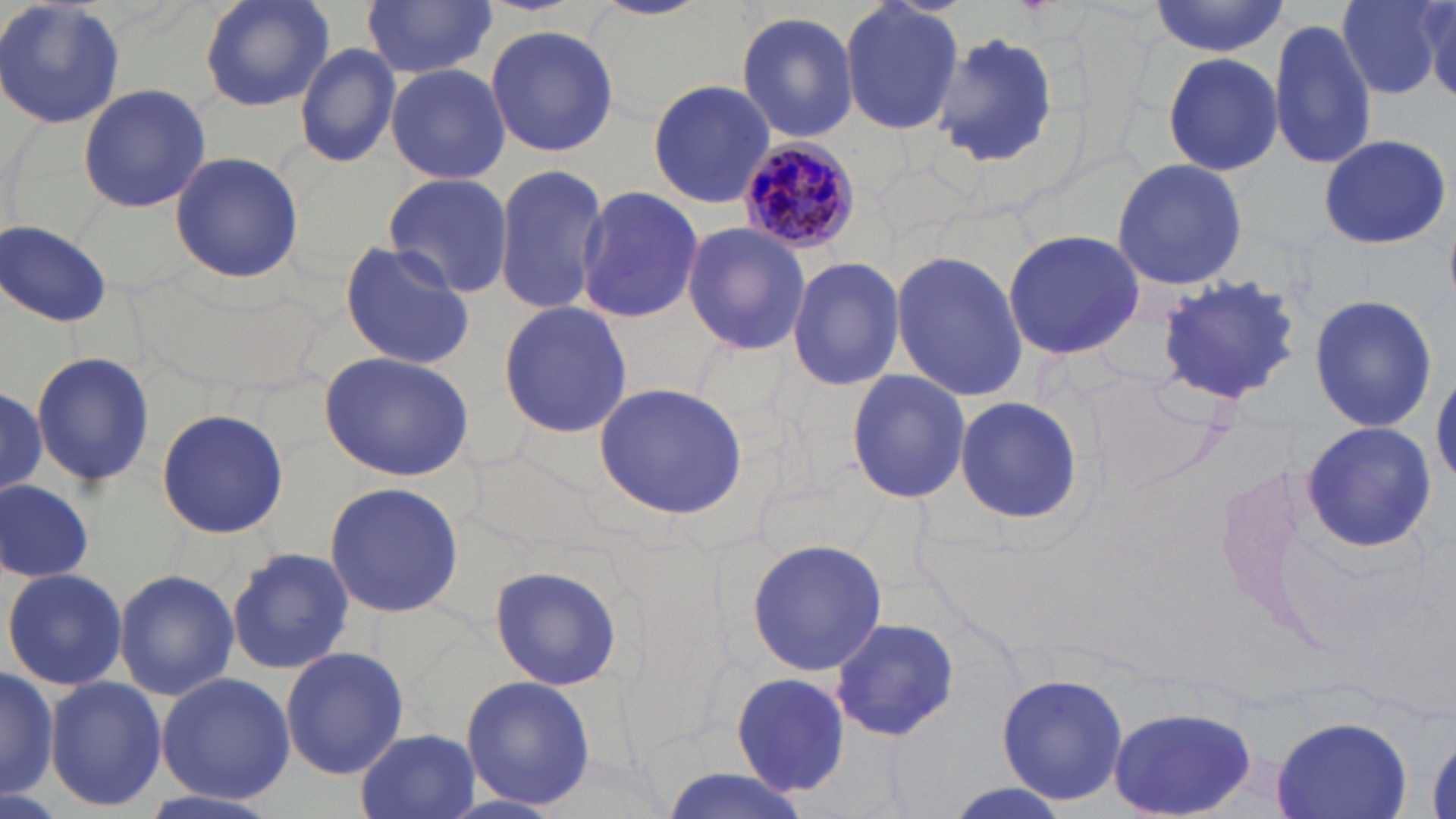

Approximate bounding boxes as (x1,y1)-(x2,y2) corner pairs in pixels. Plasmodium malariae-infected red blood cell locations: (733,138)-(863,256). Uninfected red blood cell locations: (0,0)-(126,133), (195,0)-(336,113), (361,0)-(495,80), (587,0)-(713,20), (839,0)-(965,139), (1337,0)-(1449,99), (1147,1)-(1290,57), (734,11)-(861,140), (1267,16)-(1376,172), (485,25)-(620,157), (930,32)-(1064,173), (293,42)-(401,169), (1161,50)-(1283,175), (384,63)-(511,185), (647,78)-(775,210), (76,83)-(211,213), (1316,135)-(1451,250), (168,150)-(304,286), (1110,159)-(1248,289), (492,163)-(611,318), (381,173)-(514,298), (575,185)-(704,325), (2,219)-(114,327), (681,222)-(811,357), (1001,230)-(1145,360), (337,241)-(475,371), (889,250)-(1028,403), (786,253)-(907,391), (1154,276)-(1305,405), (1308,294)-(1438,433), (496,302)-(633,437), (319,349)-(477,480), (30,350)-(158,488), (845,369)-(972,505), (1432,370)-(1456,485), (593,384)-(750,518), (0,390)-(48,493), (954,395)-(1083,525), (156,407)-(291,541), (1302,422)-(1435,549), (0,477)-(95,585), (322,481)-(467,621), (746,537)-(887,677), (227,546)-(354,676), (487,566)-(624,690), (4,567)-(127,691), (113,568)-(238,701), (829,616)-(958,740), (280,644)-(410,781), (0,663)-(60,799), (994,670)-(1130,807), (155,671)-(296,803), (731,673)-(850,796), (42,676)-(166,813), (461,676)-(597,812), (1107,707)-(1259,819), (1270,716)-(1413,819), (355,729)-(479,818), (655,769)-(814,819), (129,786)-(287,819). Slide-level diagnosis: Plasmodium malariae. One field of a larger specimen. Image is 1456×819 pixels. Thin blood smear. Captured at 1000x magnification. Optical microscopy. May-Grünwald-Giemsa-stained preparation.